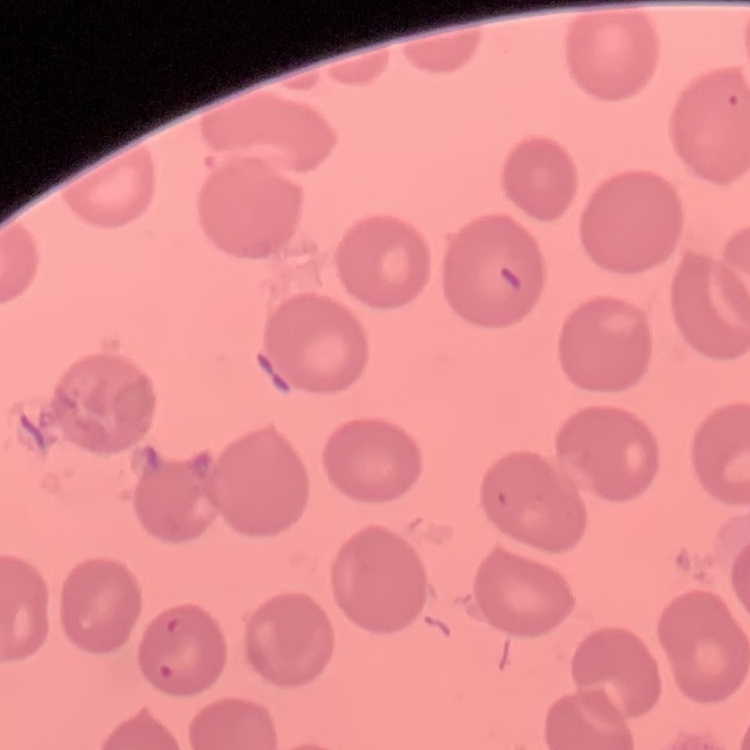
Summary:
  - Red blood cell morphology: no rouleaux formation
  - Image type: square crop of a larger photomicrograph
  - Stain: Field's or Giemsa
  - Preparation: thin blood smear